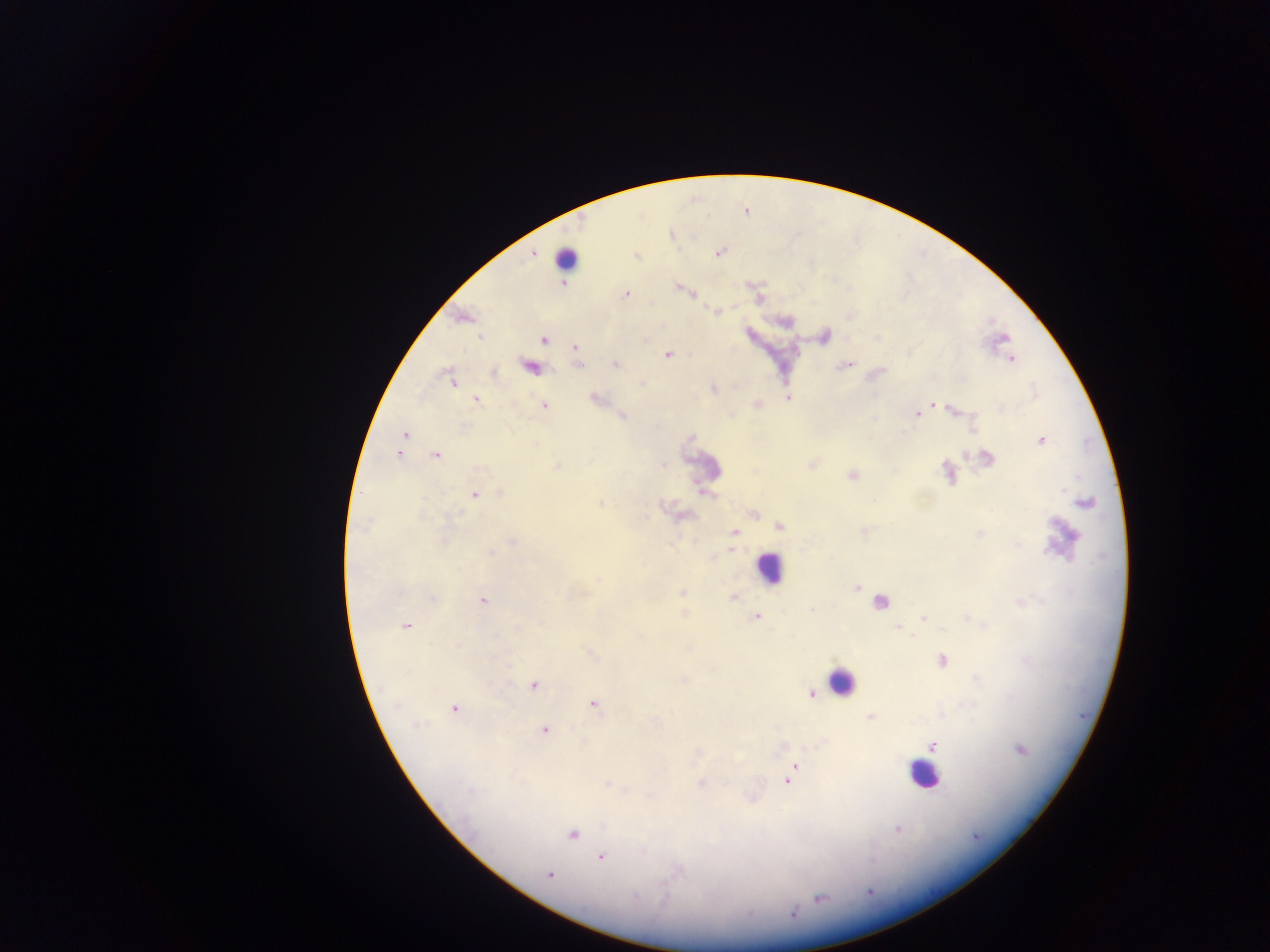

{
  "field_of_view": "single",
  "country": "Ghana",
  "capture": "mobile-phone photograph through a microscope",
  "leukocyte_locations": "approximate centers as x y in pixels: 565 258; 704 468; 768 568; 842 681; 923 774",
  "malaria_parasite_locations": "approximate centers as x y in pixels: 534 252; 719 252; 637 256; 563 282; 678 288; 626 294; 693 295; 758 298; 716 311; 462 318; 480 336; 824 337; 543 340; 575 346; 667 355; 1011 358; 614 364; 846 364; 530 367; 493 372; 451 379; 713 389; 595 397; 788 397; 476 399; 757 403; 934 404; 543 405; 951 410; 915 414; 622 416; 405 435; 1041 440; 399 454; 436 455; 986 458; 662 464; 812 464; 557 466; 852 474; 947 474; 473 495; 599 503; 1084 503; 753 514; 778 525; 734 533; 979 534; 512 543; 856 587; 682 592; 432 597; 733 597; 482 600; 880 602; 684 614; 756 616; 924 617; 406 625; 898 628; 941 661; 683 678; 534 685; 813 693; 593 703; 454 708; 871 718; 543 730; 933 745; 1020 749; 793 766; 787 779; 606 783; 701 783; 899 828; 571 834; 601 856; 550 874; 820 899; 792 914",
  "preparation": "thick blood film",
  "image_size": "1270×952 pixels"
}